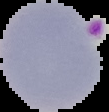

From a thin blood smear. Result: Plasmodium parasites identified. The area outside the segmented cell region is set to black. Image is 109×112 pixels.